Identify the cell.
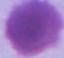
This is an erythrocyte.

1000x magnification. Micrograph.